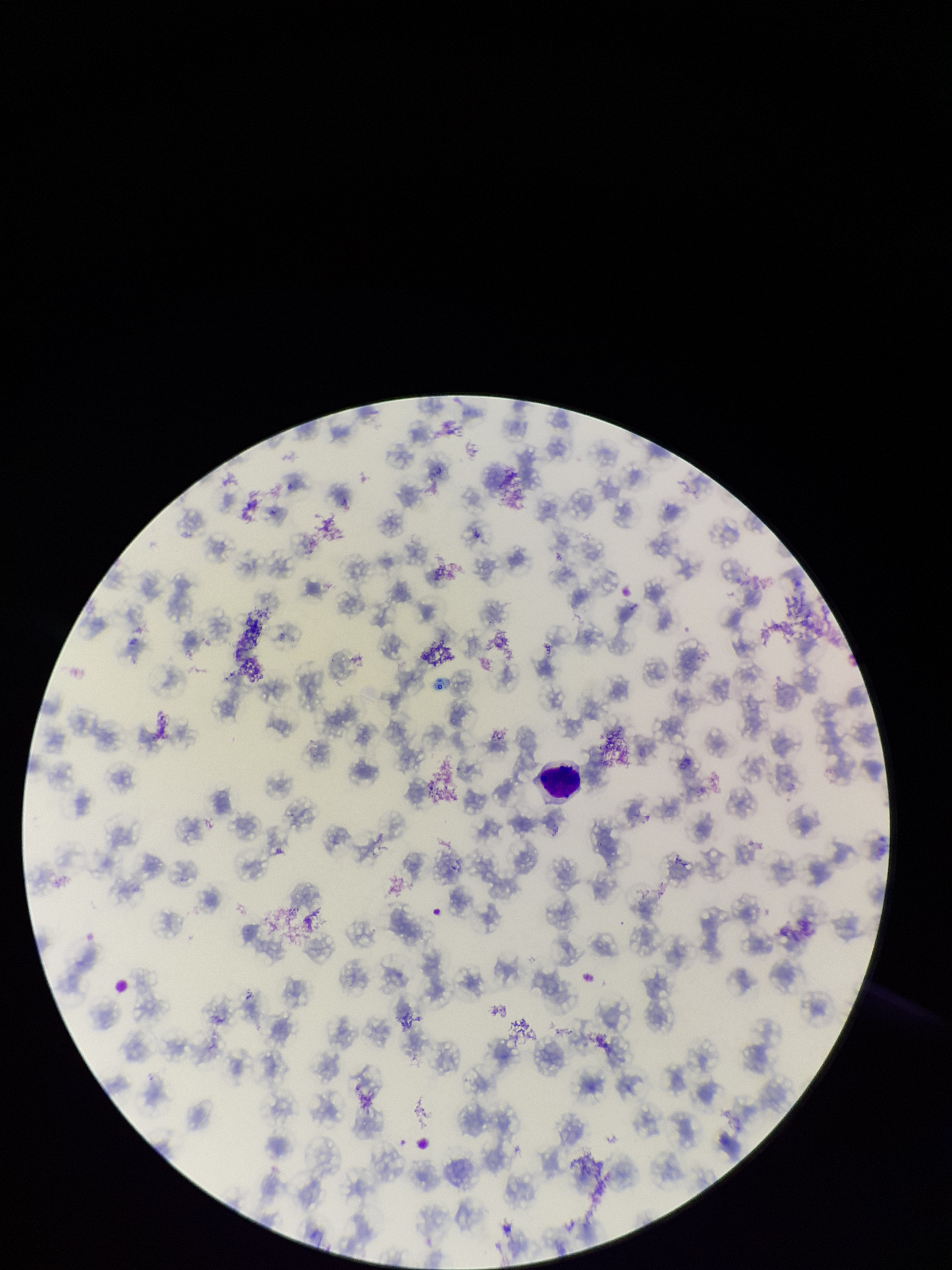
Stained with Giemsa. Patient malaria status: infected. Parasitized red blood cell count: 0. Single field of view. Image is 952×1270 pixels. Species reported for this patient: Plasmodium falciparum. Preparation: thin blood smear. Parasitized red blood cells: none seen. Smartphone photograph taken through the eyepiece of a microscope. Red blood cell count: 107.